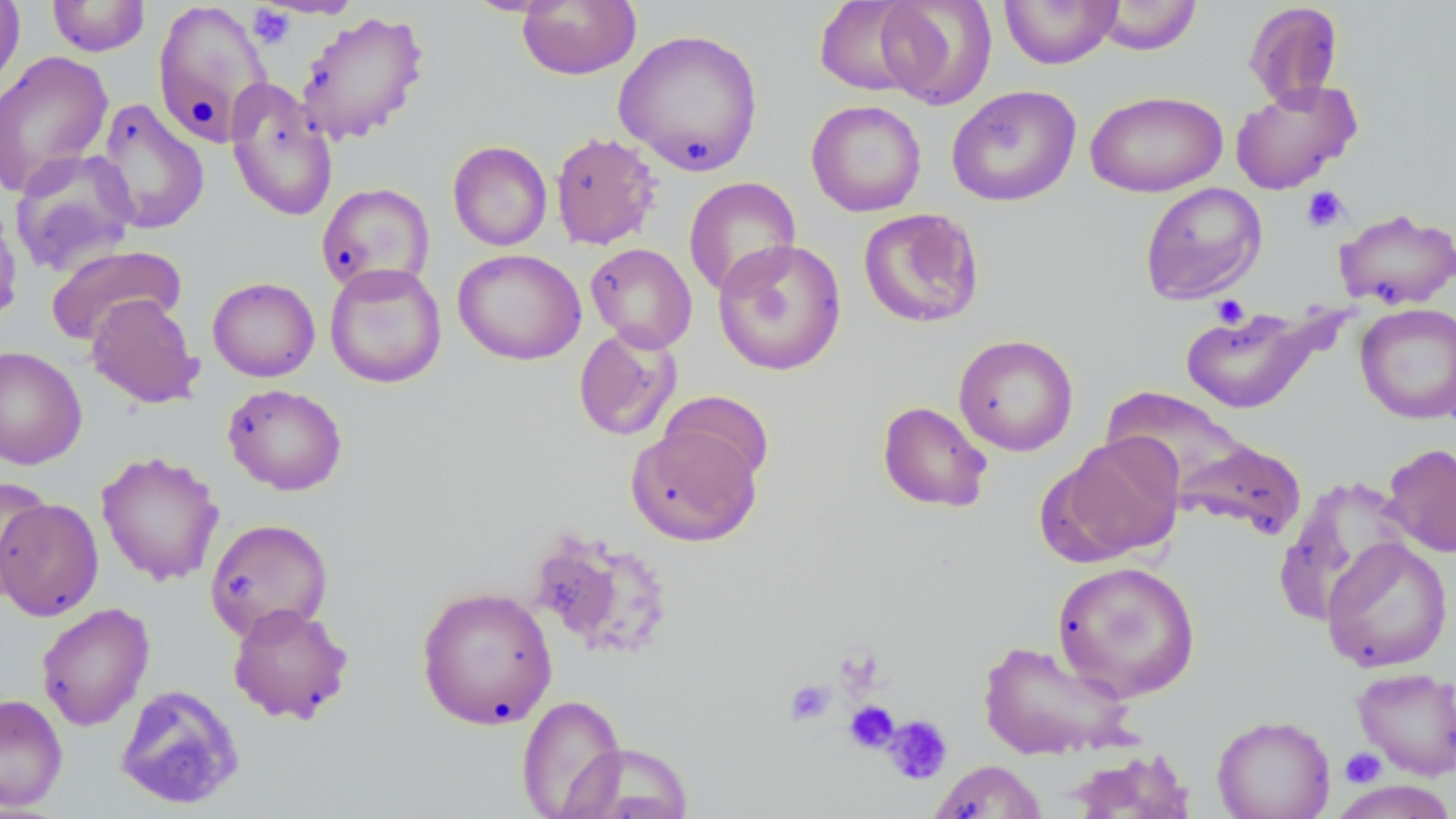

slide_level_diagnosis: no evidence of blood parasites
modality: light microscopy
field_of_view: single
preparation: thin blood smear
stain: May-Grünwald-Giemsa
platelet_locations: 'approximate bounding boxes as (x1, y1, x2, y2) in pixels: (247, 4, 295, 49), (1300, 185, 1350, 233), (1210, 295, 1251, 329), (834, 646, 886, 700), (783, 678, 836, 727), (844, 700, 900, 754), (882, 715, 953, 784), (1340, 747, 1387, 788)'
image_size: 1456×819 pixels
magnification: 1000x
uninfected_red_blood_cell_locations: 'approximate bounding boxes as (x1, y1, x2, y2) in pixels: (0, 0, 26, 96), (46, 0, 151, 57), (516, 0, 641, 81), (814, 0, 929, 97), (875, 0, 997, 109), (999, 0, 1123, 68), (151, 1, 273, 148), (1092, 1, 1203, 55), (1243, 2, 1344, 108), (294, 10, 430, 145), (612, 28, 765, 177), (0, 50, 114, 198), (224, 78, 338, 222), (1229, 79, 1362, 195), (945, 85, 1082, 207), (1085, 90, 1228, 197), (94, 98, 210, 236), (806, 99, 927, 217), (549, 131, 663, 250), (448, 140, 553, 251), (10, 148, 140, 278), (683, 177, 801, 297), (316, 182, 434, 295), (1139, 182, 1267, 305), (0, 197, 23, 330), (1333, 207, 1456, 311), (858, 208, 985, 329), (712, 238, 848, 376), (586, 242, 697, 353), (46, 244, 186, 346), (453, 248, 585, 365), (324, 263, 447, 388), (208, 277, 320, 381), (85, 293, 203, 409), (1355, 302, 1456, 425), (1179, 305, 1326, 414), (573, 326, 683, 442), (953, 334, 1078, 456), (0, 346, 87, 470), (223, 383, 348, 496), (1103, 387, 1255, 501), (660, 390, 775, 487), (876, 401, 993, 513), (626, 422, 762, 546), (1053, 436, 1185, 562), (1174, 438, 1306, 538), (1381, 443, 1456, 558), (96, 450, 225, 586), (1274, 475, 1415, 624), (0, 478, 53, 600), (1, 498, 103, 622), (205, 518, 334, 642), (1321, 537, 1453, 673), (1051, 560, 1201, 702), (416, 585, 558, 730), (36, 602, 154, 731), (227, 602, 354, 725), (975, 639, 1137, 761), (1351, 666, 1455, 780), (114, 684, 245, 810), (0, 693, 68, 812), (516, 694, 627, 818), (1212, 714, 1336, 819), (563, 743, 696, 819), (1063, 748, 1197, 818), (928, 760, 1048, 818), (1327, 779, 1456, 818)'